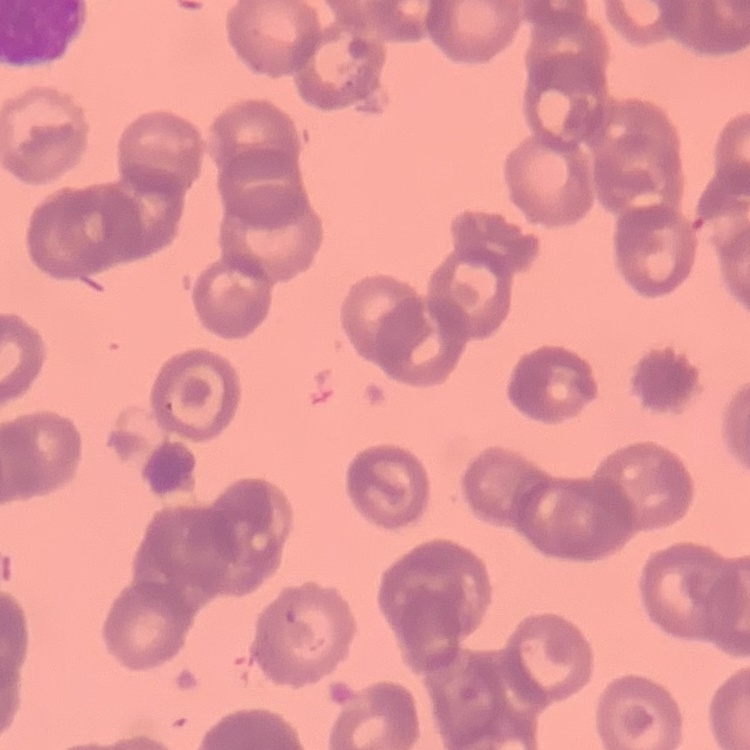 The red blood cells show rouleaux formation. Field's or Giemsa stain. Thin peripheral smear. Square crop of a larger photomicrograph.